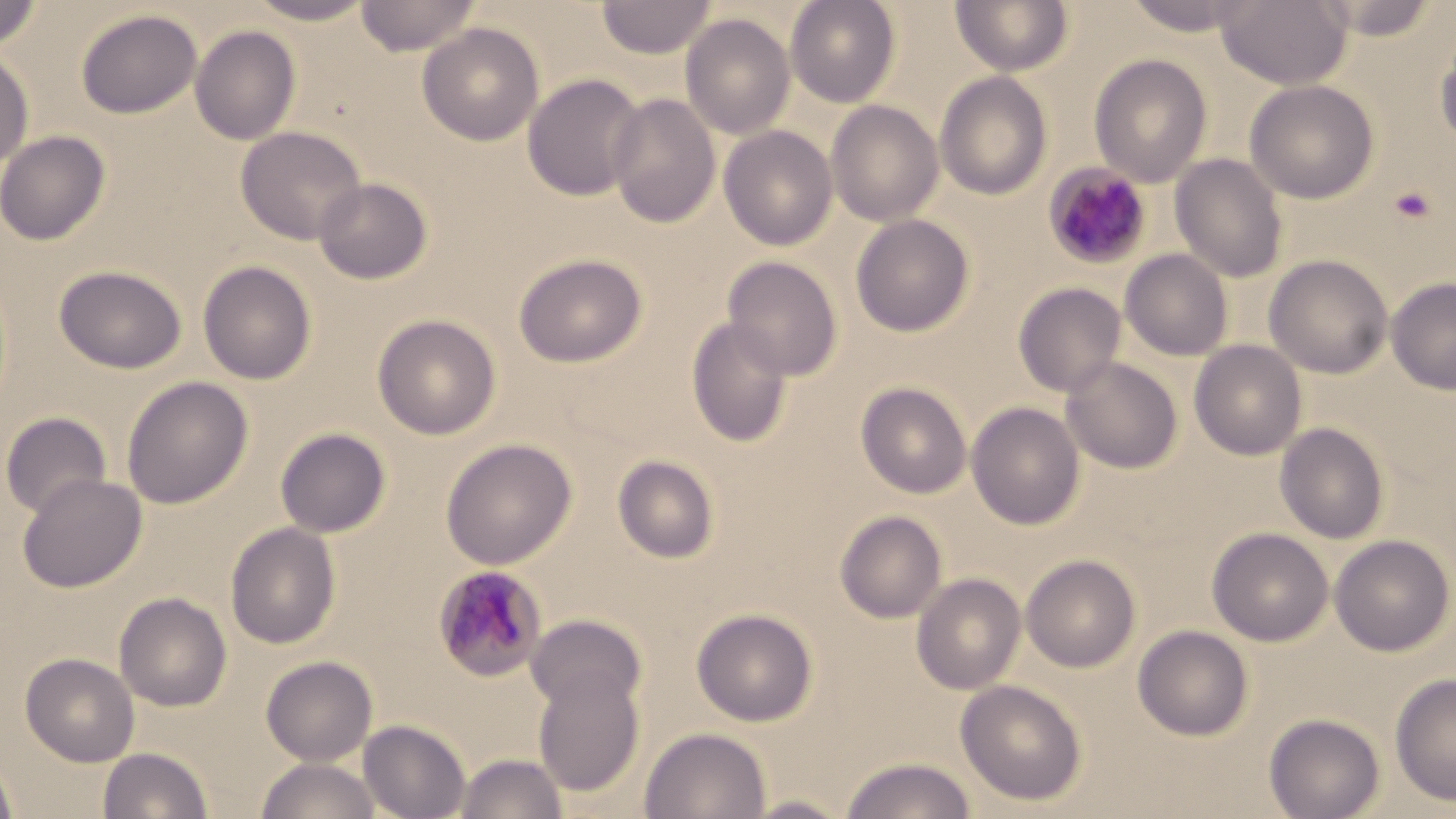

Summary:
  - Coordinate format: approximate bounding boxes as [x1, y1, x2, y2] in pixels
  - Platelet locations: [1389, 186, 1436, 223]
  - Uninfected red blood cell locations: [248, 0, 375, 25], [356, 0, 481, 56], [596, 0, 717, 59], [785, 0, 901, 107], [950, 0, 1073, 76], [1122, 0, 1259, 37], [1216, 0, 1353, 89], [1313, 0, 1443, 40], [0, 1, 44, 52], [75, 9, 203, 119], [680, 13, 796, 140], [417, 22, 544, 146], [190, 25, 301, 145], [1435, 29, 1456, 147], [0, 48, 34, 169], [1089, 54, 1213, 187], [935, 71, 1053, 200], [522, 73, 647, 202], [1244, 79, 1380, 204], [606, 92, 721, 228], [826, 100, 944, 226], [719, 125, 838, 250], [236, 126, 367, 245], [0, 130, 110, 246], [1170, 154, 1289, 283], [313, 177, 433, 285], [851, 214, 975, 337], [1120, 249, 1233, 361], [513, 253, 647, 368], [722, 255, 842, 380], [1264, 255, 1393, 379], [197, 260, 318, 385], [53, 264, 187, 374], [1386, 277, 1456, 395], [1013, 282, 1127, 398], [373, 314, 501, 440], [685, 317, 794, 447], [1189, 340, 1307, 460], [1062, 357, 1183, 474], [121, 376, 254, 509], [856, 382, 972, 498], [966, 401, 1085, 530], [0, 411, 113, 519], [1275, 422, 1389, 544], [275, 427, 391, 538], [440, 438, 578, 570], [612, 454, 719, 564], [17, 472, 147, 593], [834, 510, 947, 624], [225, 522, 342, 649], [1207, 527, 1334, 646], [1330, 534, 1454, 656], [1021, 554, 1141, 673], [911, 573, 1026, 695], [114, 592, 232, 712], [691, 607, 818, 726], [526, 614, 647, 715], [1132, 625, 1254, 741], [20, 652, 140, 766], [261, 655, 378, 765], [532, 664, 646, 798], [1389, 672, 1456, 806], [955, 679, 1087, 806], [1264, 713, 1385, 819], [358, 719, 470, 819], [639, 727, 772, 819], [98, 747, 213, 819], [454, 753, 568, 819], [0, 755, 18, 819], [841, 756, 975, 818], [257, 757, 381, 818], [741, 794, 854, 818]
  - Plasmodium malariae-infected red blood cell locations: [1043, 162, 1152, 270], [432, 565, 548, 683]
  - Slide-level diagnosis: Plasmodium malariae
  - Image size: 1456×819 pixels
  - Field of view: single
  - Magnification: 1000x
  - Modality: optical microscopy
  - Preparation: thin blood smear
  - Stain: May-Grünwald-Giemsa